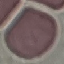

Result: no malaria parasites detected. Automatically extracted cell patch, resized to 64 × 64 pixels. Thin smear of blood. Photographed with a smartphone camera at the microscope eyepiece. Giemsa-stained preparation.